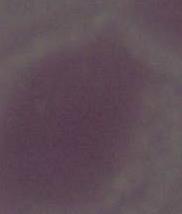
modality = micrograph
identification = red blood cell
magnification = 1000x